Assess this cell for malaria.
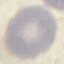
Uninfected.

Summary:
  - Stain: Giemsa
  - Image type: automatically extracted cell patch, resized to 64 × 64 pixels
  - Preparation: thin blood film
  - Capture: smartphone camera at the microscope eyepiece